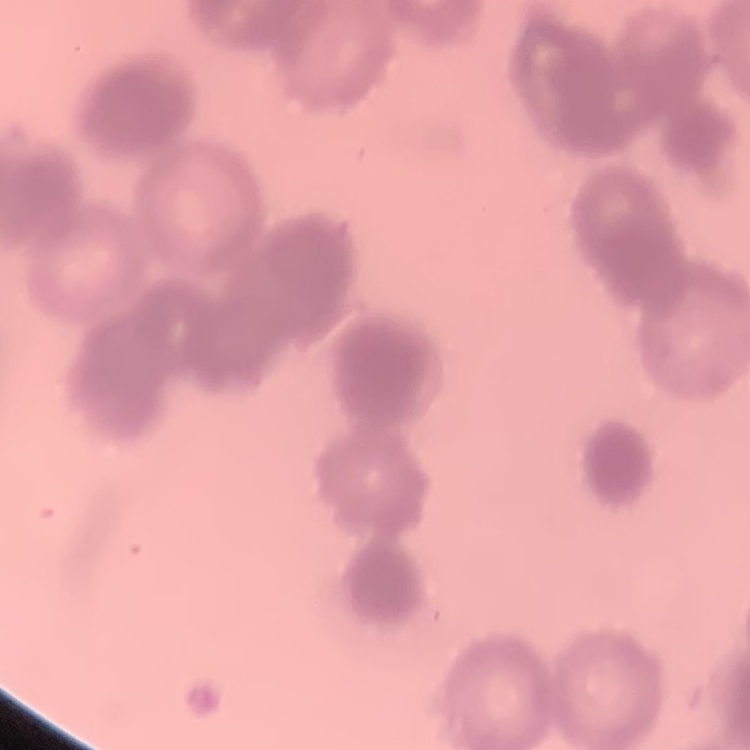
Summary:
  - Erythrocyte morphology: rouleaux formation
  - Image type: one tile cut from a larger photomicrograph
  - Stain: Field's or Giemsa
  - Preparation: thin blood smear